Name the parasite shown.
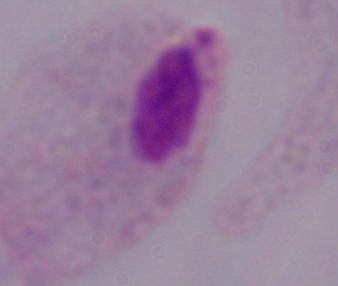
A trichomonad.

1000x magnification. Micrograph.